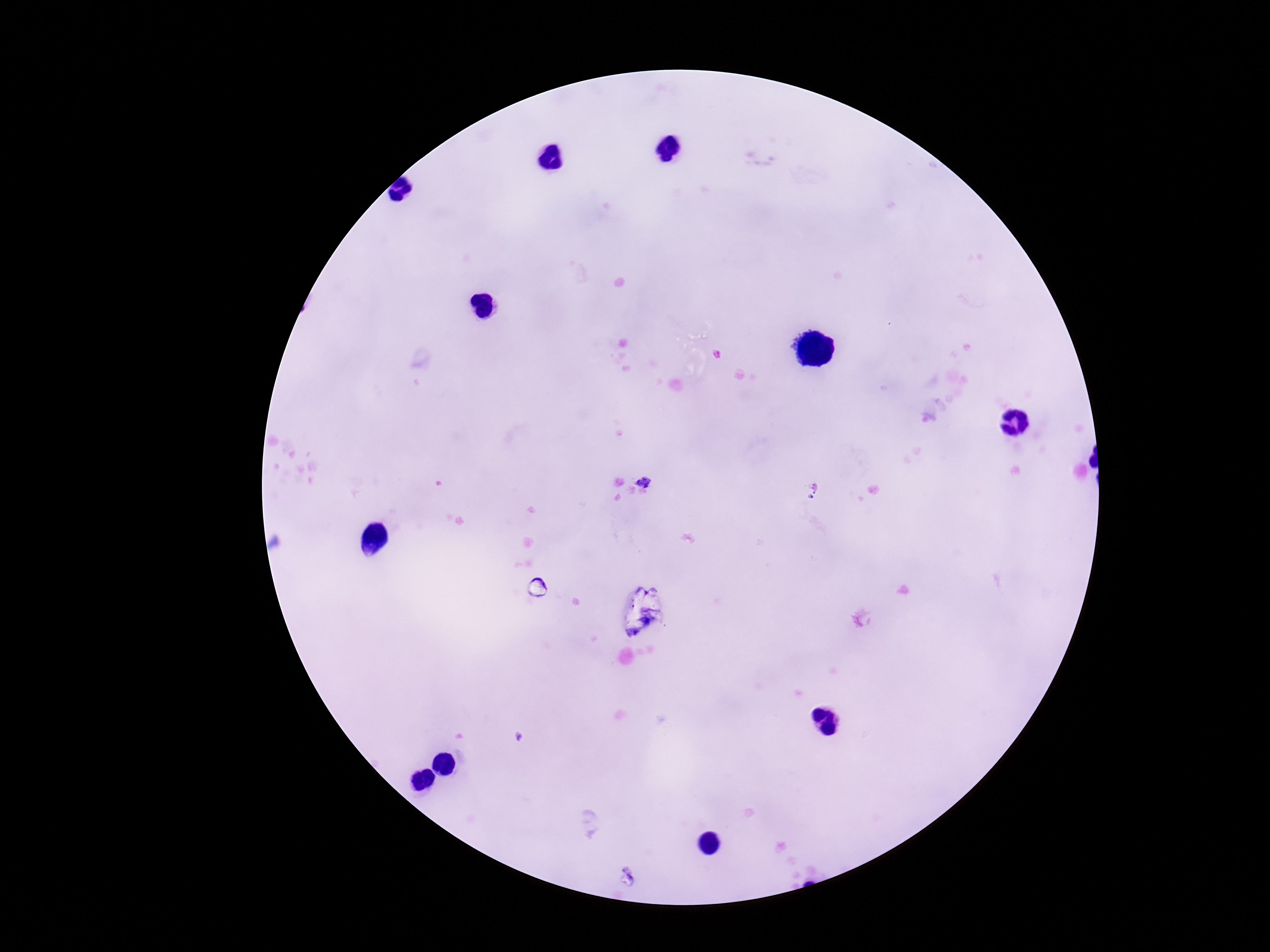 Approximate centers as [x, y] in pixels. Plasmodium parasite locations: [646, 483]. Thick blood smear. Image is 1270×952 pixels. Patient malaria status: infected. Smartphone photograph taken through the microscope eyepiece. Giemsa stain. Single field of view. 100x magnification.